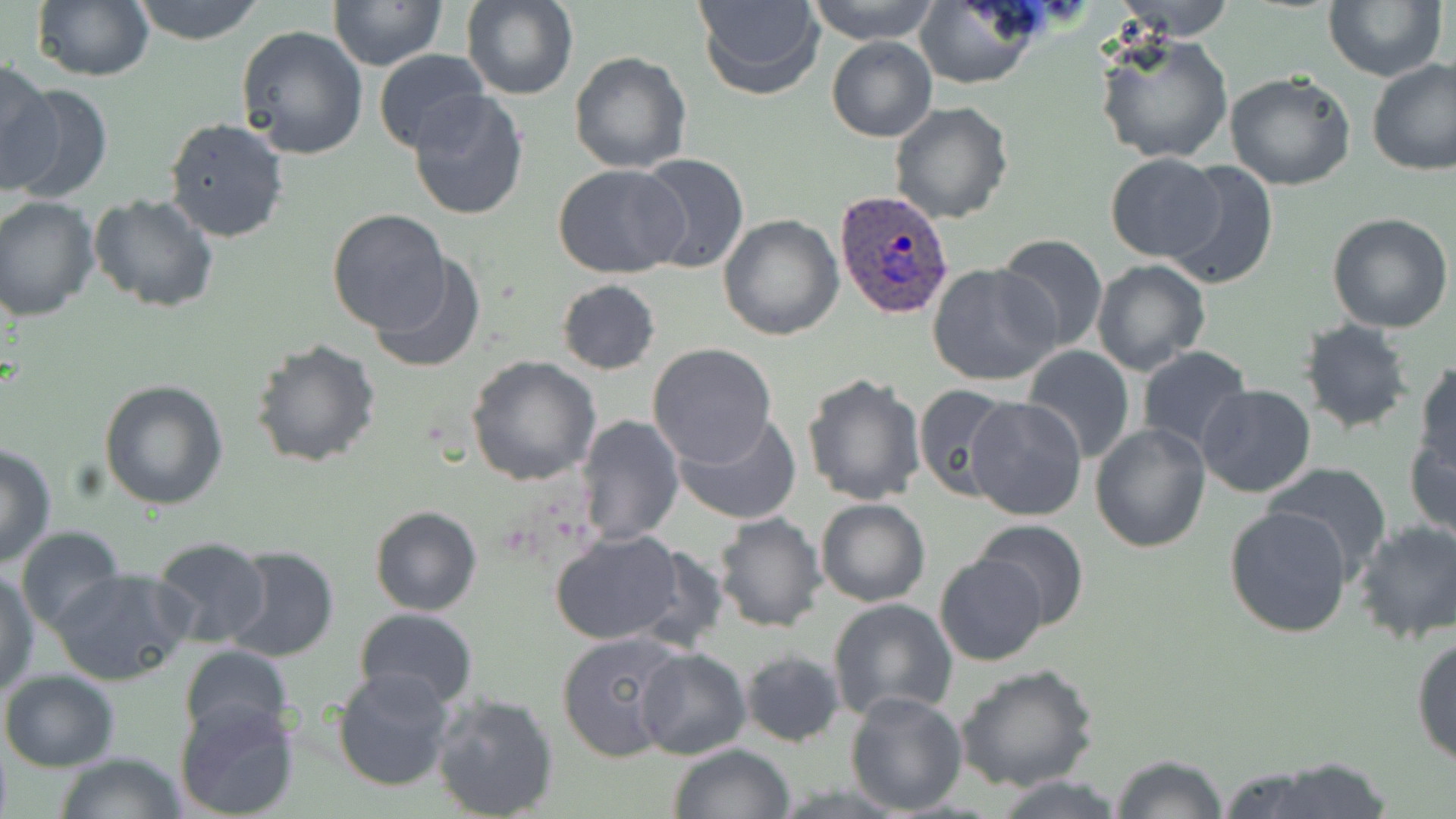 Approximate bounding boxes as (x1,y1)-(x2,y2) corner pairs in pixels. Plasmodium ovale-infected red blood cell locations: (833,189)-(955,320). Uninfected red blood cell locations: (131,0)-(266,44), (327,0)-(448,71), (692,0)-(825,99), (806,0)-(941,43), (913,0)-(1039,89), (1112,0)-(1238,41), (1324,0)-(1448,81), (461,1)-(579,101), (31,2)-(154,81), (236,25)-(368,159), (1094,30)-(1235,165), (826,37)-(936,142), (372,49)-(492,157), (568,52)-(691,172), (1366,58)-(1456,176), (0,60)-(59,193), (1225,70)-(1356,190), (6,85)-(114,204), (406,90)-(529,221), (889,101)-(1014,223), (163,117)-(291,242), (1105,152)-(1223,263), (634,154)-(748,275), (552,162)-(686,279), (1163,162)-(1279,290), (88,194)-(219,313), (0,197)-(99,321), (327,208)-(450,332), (1327,212)-(1455,333), (718,213)-(843,340), (993,232)-(1108,354), (369,253)-(487,376), (1091,259)-(1213,377), (928,263)-(1058,386), (555,279)-(661,374), (1298,319)-(1416,436), (249,337)-(383,468), (647,343)-(778,467), (1021,344)-(1136,463), (1135,345)-(1253,454), (466,356)-(602,485), (1413,362)-(1456,480), (801,372)-(929,506), (98,379)-(229,511), (912,383)-(1014,502), (1195,384)-(1317,498), (966,397)-(1088,520), (673,409)-(802,526), (575,414)-(683,544), (1090,421)-(1213,553), (1405,430)-(1456,541), (0,443)-(56,569), (1264,463)-(1394,582), (814,498)-(931,606), (1224,504)-(1353,638), (369,505)-(483,617), (713,511)-(828,633), (971,519)-(1091,632), (1351,519)-(1456,645), (16,526)-(126,634), (548,529)-(689,646), (148,536)-(272,648), (221,546)-(340,664), (935,552)-(1048,665), (49,568)-(194,685), (1,571)-(40,696), (828,596)-(958,723), (353,607)-(478,709), (1410,630)-(1456,768), (557,631)-(690,761), (178,644)-(294,746), (636,646)-(752,760), (739,648)-(847,748), (956,665)-(1099,793), (330,666)-(456,793), (1,669)-(121,771), (843,689)-(967,814), (430,690)-(560,819), (174,699)-(302,818), (668,743)-(795,819), (55,752)-(186,818), (1109,754)-(1230,818), (1222,756)-(1400,819), (990,776)-(1133,818). Slide-level diagnosis: Plasmodium ovale. May-Grünwald-Giemsa stain. Captured at 1000x magnification. Thin blood smear. Light microscopy. Image is 1456×819 pixels. One field of a larger specimen.